Classify this cell by malaria status.
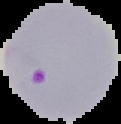
Parasitized.

{
  "preparation": "thin blood smear",
  "image_type": "segmented cell region with the area outside set to black",
  "image_size": "121×124 pixels"
}